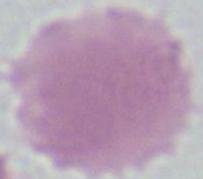
Summary:
  - Identification: red blood cell
  - Magnification: 1000x
  - Modality: micrograph